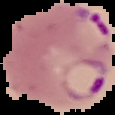
Summary:
  - Image size: 115×115 pixels
  - Image type: segmented cell region on a black background
  - Malaria status: parasitized
  - Preparation: thin blood smear